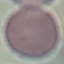
Malaria status: uninfected. Giemsa stain. Cell patch, automatically extracted from a larger field of view and resized to 64 × 64 pixels. Thin smear of blood. Acquired by smartphone through the microscope eyepiece.